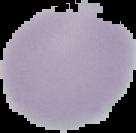
Summary:
  - Image size: 136×133 pixels
  - Malaria status: uninfected
  - Image type: segmented cell region with the area outside set to black
  - Preparation: thin blood film